Give the position of every Plasmodium parasite.
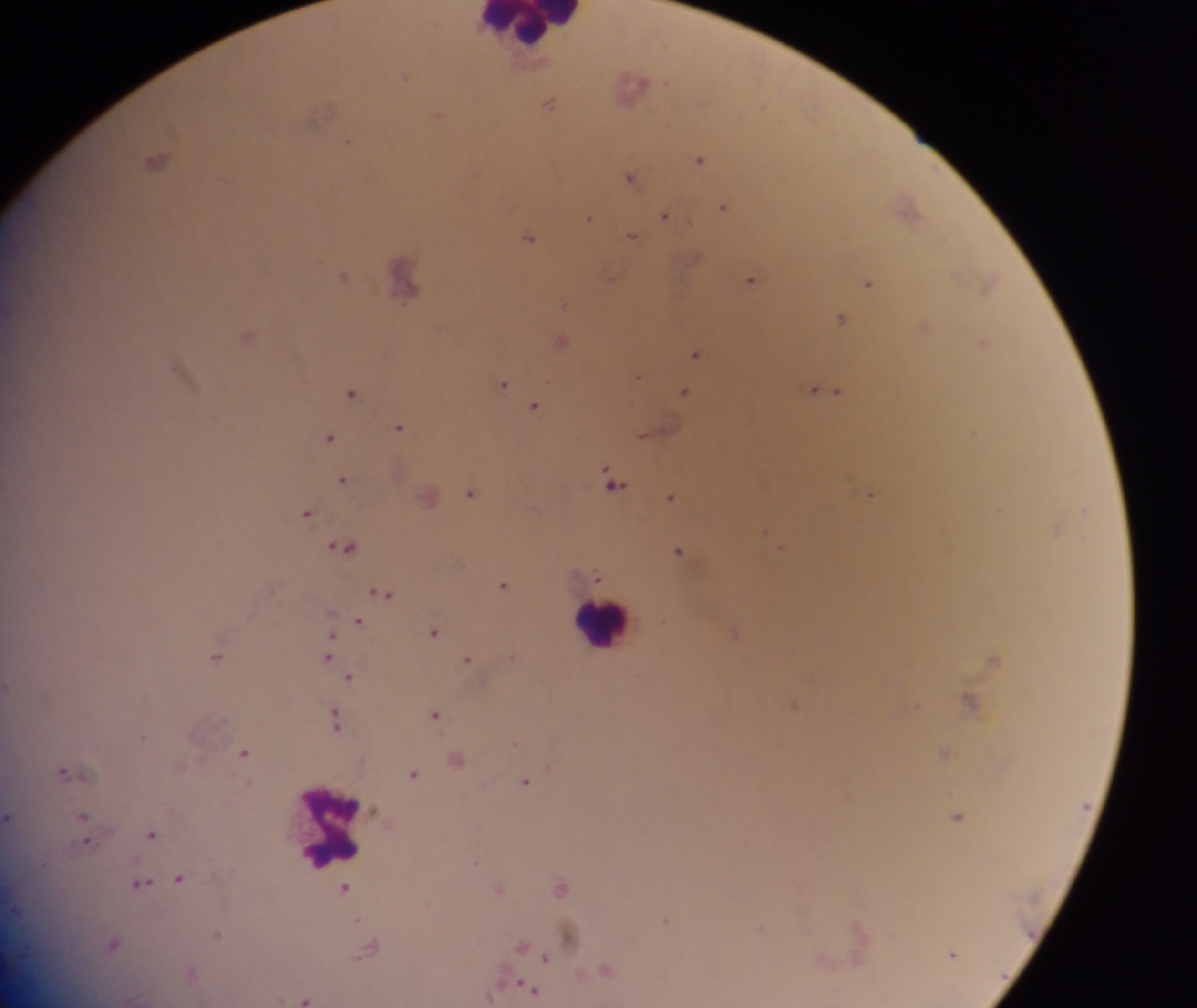

Approximate centers as (x, y) in pixels.
Plasmodium parasites: (404, 75), (632, 86), (549, 101), (321, 112), (439, 115), (346, 141), (700, 158), (157, 160), (630, 176), (907, 203), (724, 205), (664, 215), (588, 217), (631, 234), (529, 236), (343, 276), (403, 276), (610, 276), (750, 278), (867, 282), (987, 282), (840, 318), (924, 325), (248, 334), (561, 340), (984, 341), (695, 353), (637, 375), (503, 383), (819, 389), (685, 391), (837, 391), (351, 392), (534, 406), (399, 427), (973, 432), (642, 435), (329, 437), (342, 479), (613, 483), (470, 491), (869, 492), (671, 496), (1085, 510), (306, 513), (1055, 528), (765, 532), (345, 546), (679, 550), (597, 576), (503, 584), (382, 592), (359, 621), (433, 631), (216, 655), (328, 656), (993, 658), (468, 659), (350, 676), (969, 698), (917, 705), (435, 714), (335, 720), (143, 736), (514, 741), (244, 751), (945, 752), (457, 759), (65, 771), (414, 773), (525, 781), (82, 816), (957, 816), (9, 817), (85, 831), (152, 833), (475, 862), (180, 878), (140, 883), (561, 887), (345, 888), (500, 888), (358, 920), (666, 920), (569, 934), (112, 943), (522, 944), (368, 948), (951, 953), (546, 957), (607, 969), (526, 987), (304, 998).

Leukocyte locations: (532, 27), (603, 623), (334, 826). Mobile-phone photograph taken through the microscope. Thick blood smear. Sample from Ghana. Image is 1197×1008 pixels. One field of view.